Classify this cell by malaria status.
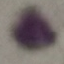

It is uninfected.

{
  "preparation": "thin blood film",
  "image_type": "automatically extracted cell patch, resized to 64 × 64 pixels",
  "capture": "smartphone camera at the microscope eyepiece",
  "stain": "Giemsa"
}